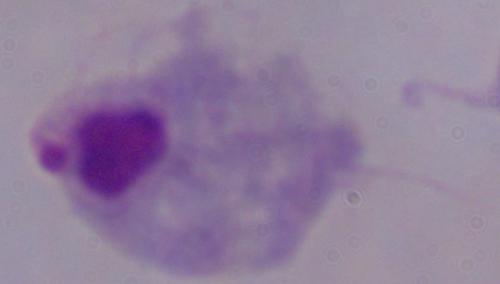 A trichomonad is shown. Photomicrograph. Captured at 1000x magnification.